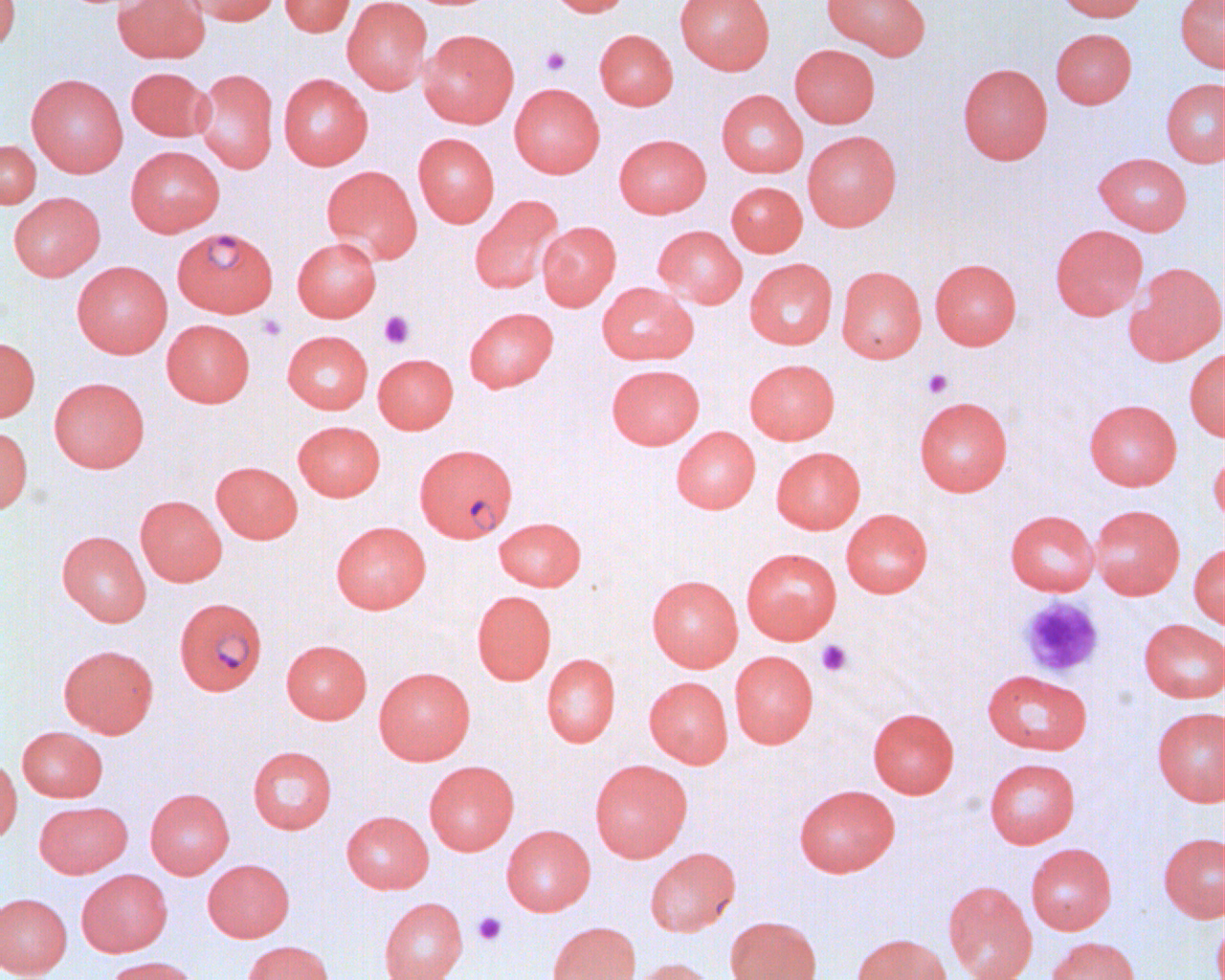 Approximate bounding boxes as [x1, y1, x2, y2] in pixels. Plasmodium falciparum-infected red blood cell locations: [174, 228, 279, 319], [414, 442, 517, 542], [174, 597, 267, 695]. Platelet locations: [540, 46, 571, 76], [379, 311, 415, 349], [256, 314, 287, 342], [921, 368, 953, 398], [1018, 596, 1104, 678], [815, 639, 853, 677], [472, 912, 507, 945]. Uninfected red blood cell locations: [0, 0, 21, 53], [113, 0, 210, 63], [183, 0, 280, 25], [279, 0, 355, 37], [342, 0, 432, 94], [546, 0, 632, 17], [675, 0, 775, 74], [821, 0, 932, 60], [1056, 0, 1149, 22], [1174, 0, 1225, 73], [1051, 28, 1137, 109], [419, 29, 519, 128], [594, 29, 678, 110], [789, 44, 880, 128], [957, 63, 1053, 164], [126, 66, 212, 142], [193, 69, 279, 173], [26, 73, 128, 177], [278, 73, 372, 170], [1160, 78, 1224, 167], [509, 83, 605, 178], [716, 89, 807, 178], [802, 130, 902, 231], [413, 133, 500, 227], [614, 134, 711, 218], [0, 140, 41, 208], [126, 145, 225, 236], [1094, 152, 1192, 235], [322, 165, 421, 263], [726, 181, 807, 256], [9, 192, 105, 280], [470, 195, 563, 295], [537, 221, 621, 310], [1050, 224, 1148, 320], [653, 225, 746, 308], [292, 237, 382, 321], [744, 258, 837, 349], [930, 258, 1021, 350], [71, 261, 173, 358], [1125, 262, 1225, 365], [836, 266, 926, 363], [597, 282, 698, 365], [464, 307, 558, 392], [162, 319, 255, 407], [282, 330, 373, 414], [0, 337, 40, 422], [1184, 347, 1225, 442], [373, 353, 458, 434], [744, 358, 839, 444], [607, 364, 704, 449], [49, 377, 149, 473], [914, 396, 1013, 496], [1083, 399, 1182, 490], [292, 420, 385, 501], [0, 426, 33, 514], [671, 426, 760, 513], [1208, 443, 1225, 528], [771, 446, 865, 534], [211, 461, 302, 543], [135, 495, 227, 586], [1089, 504, 1185, 599], [840, 508, 933, 597], [1005, 510, 1099, 596], [494, 516, 586, 591], [331, 521, 431, 613], [57, 530, 151, 626], [1189, 543, 1225, 630], [741, 548, 841, 644], [647, 575, 742, 671], [472, 590, 556, 685], [1138, 619, 1225, 703], [281, 640, 372, 724], [58, 644, 158, 738], [730, 650, 818, 748], [541, 653, 620, 747], [374, 666, 475, 765], [982, 669, 1092, 755], [644, 676, 733, 768], [1152, 706, 1225, 806], [868, 708, 959, 798], [17, 726, 107, 802], [248, 746, 337, 834], [0, 755, 22, 844], [984, 758, 1080, 848], [589, 759, 692, 862], [424, 761, 519, 855], [793, 784, 900, 877], [145, 788, 234, 878], [34, 801, 132, 878], [341, 810, 433, 894], [501, 825, 595, 916], [1158, 832, 1225, 922], [1025, 843, 1117, 935], [645, 847, 740, 936], [203, 859, 294, 942], [76, 869, 173, 956], [942, 881, 1037, 980], [0, 893, 72, 979], [378, 897, 468, 980], [1212, 906, 1225, 980], [725, 915, 822, 980], [546, 921, 641, 980], [851, 933, 951, 980], [1046, 936, 1140, 980], [241, 940, 335, 980], [104, 955, 202, 980], [630, 957, 718, 980]. Slide-level diagnosis: Plasmodium falciparum. Light microscopy. 1000x magnification. Image is 1225×980 pixels. Single field of view. Thin blood smear.